Classify this cell by malaria status.
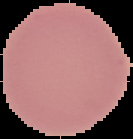
It is uninfected.

image size = 133×139 pixels
image type = segmented cell region with the area outside set to black
preparation = thin blood smear